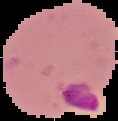
Summary:
  - Image type: cell region segmented out of the field of view; surrounding area masked to black
  - Preparation: thin blood smear
  - Malaria status: parasitized
  - Image size: 118×121 pixels